Give the position of every malaria parasite.
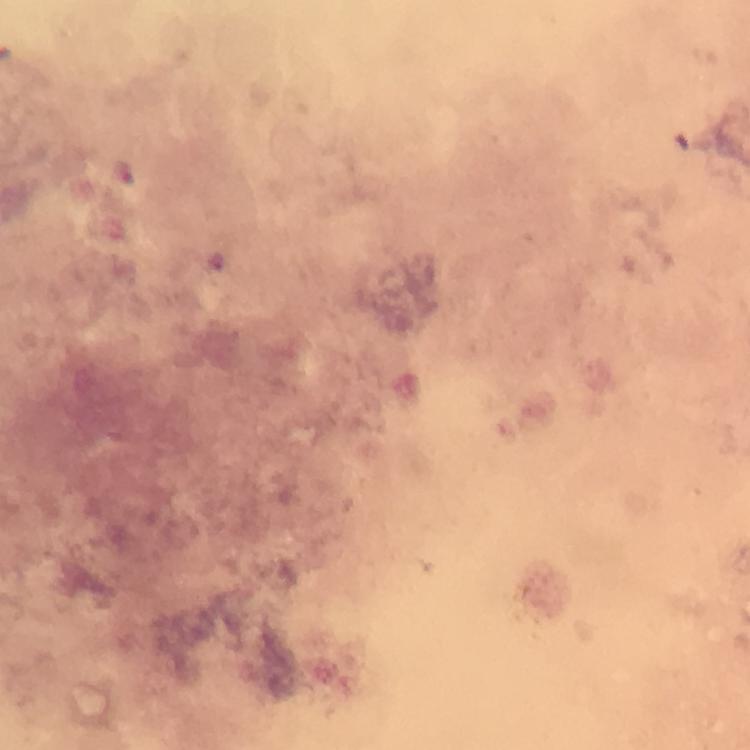
Approximate object centers, in pixels from the top-left corner.
Malaria parasites: (x=124, y=172).

Summary:
  - Immersion oil: used
  - Preparation: thick blood smear
  - Context: from a malaria diagnostic workup
  - Capture: smartphone mounted on the microscope
  - Stain: Giemsa
  - Magnification: 100x
  - Cropped from: a single field of view
  - Image size: 750×750 pixels